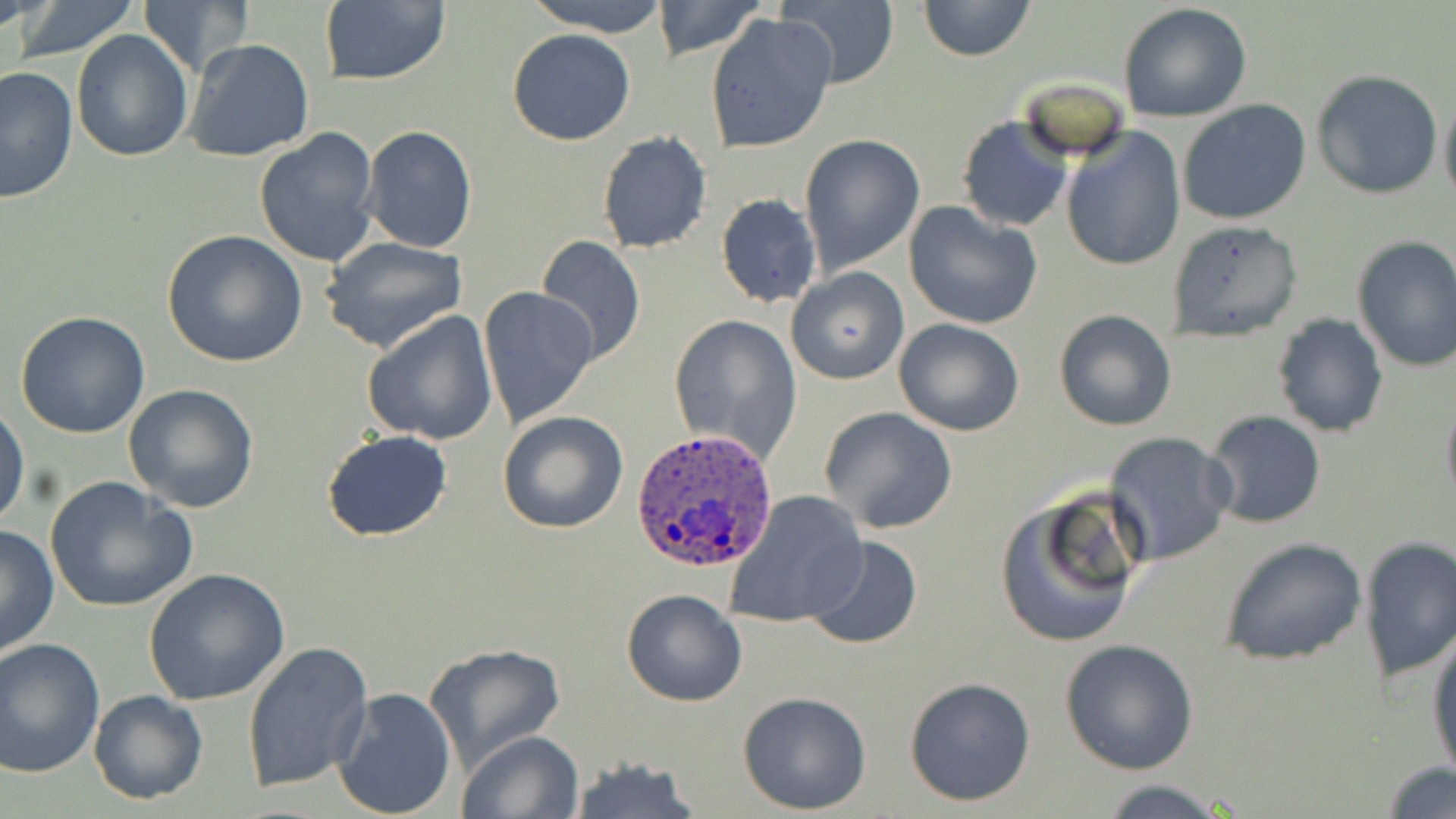

Approximate bounding boxes as (x1,y1)-(x2,y2) corner pairs in pixels. Plasmodium ovale-infected red blood cell locations: (629,429)-(778,572). Uninfected red blood cell locations: (11,0)-(145,61), (523,0)-(676,36), (650,0)-(767,60), (917,0)-(1036,63), (139,1)-(250,73), (317,1)-(453,87), (777,1)-(897,86), (1118,2)-(1254,124), (705,13)-(837,154), (507,29)-(636,146), (70,31)-(193,160), (183,38)-(316,164), (1,67)-(78,204), (1311,69)-(1444,198), (1439,90)-(1456,211), (1177,99)-(1312,225), (956,115)-(1073,233), (361,126)-(477,253), (254,127)-(380,269), (1060,128)-(1186,272), (596,132)-(712,254), (798,133)-(926,276), (708,174)-(905,301), (715,193)-(822,309), (904,200)-(1043,330), (1167,219)-(1303,342), (161,229)-(307,368), (535,234)-(646,368), (1351,235)-(1456,373), (319,236)-(470,355), (785,267)-(908,386), (478,287)-(600,431), (1052,308)-(1177,431), (360,310)-(498,447), (13,312)-(153,439), (668,312)-(803,461), (1272,313)-(1388,437), (894,318)-(1025,438), (121,383)-(261,514), (1440,391)-(1456,512), (1,403)-(27,528), (820,407)-(958,536), (1204,410)-(1326,529), (498,411)-(628,534), (322,430)-(452,542), (1104,431)-(1235,567), (44,475)-(197,615), (993,489)-(1144,648), (722,490)-(868,630), (0,523)-(59,657), (805,535)-(922,651), (1357,535)-(1456,685), (1218,536)-(1369,666), (145,567)-(290,706), (621,588)-(748,707), (1427,627)-(1456,782), (0,636)-(105,779), (1060,638)-(1201,775), (242,640)-(373,794), (423,642)-(565,772), (903,677)-(1035,806), (332,686)-(457,817), (88,689)-(209,805), (736,690)-(873,815), (458,729)-(584,819), (565,757)-(701,818), (1383,762)-(1456,817), (1090,778)-(1241,818). Slide-level diagnosis: Plasmodium ovale. Thin blood film. Image is 1456×819 pixels. Light microscopy. Single field of view. May-Grünwald-Giemsa stain. Captured at 1000x magnification.